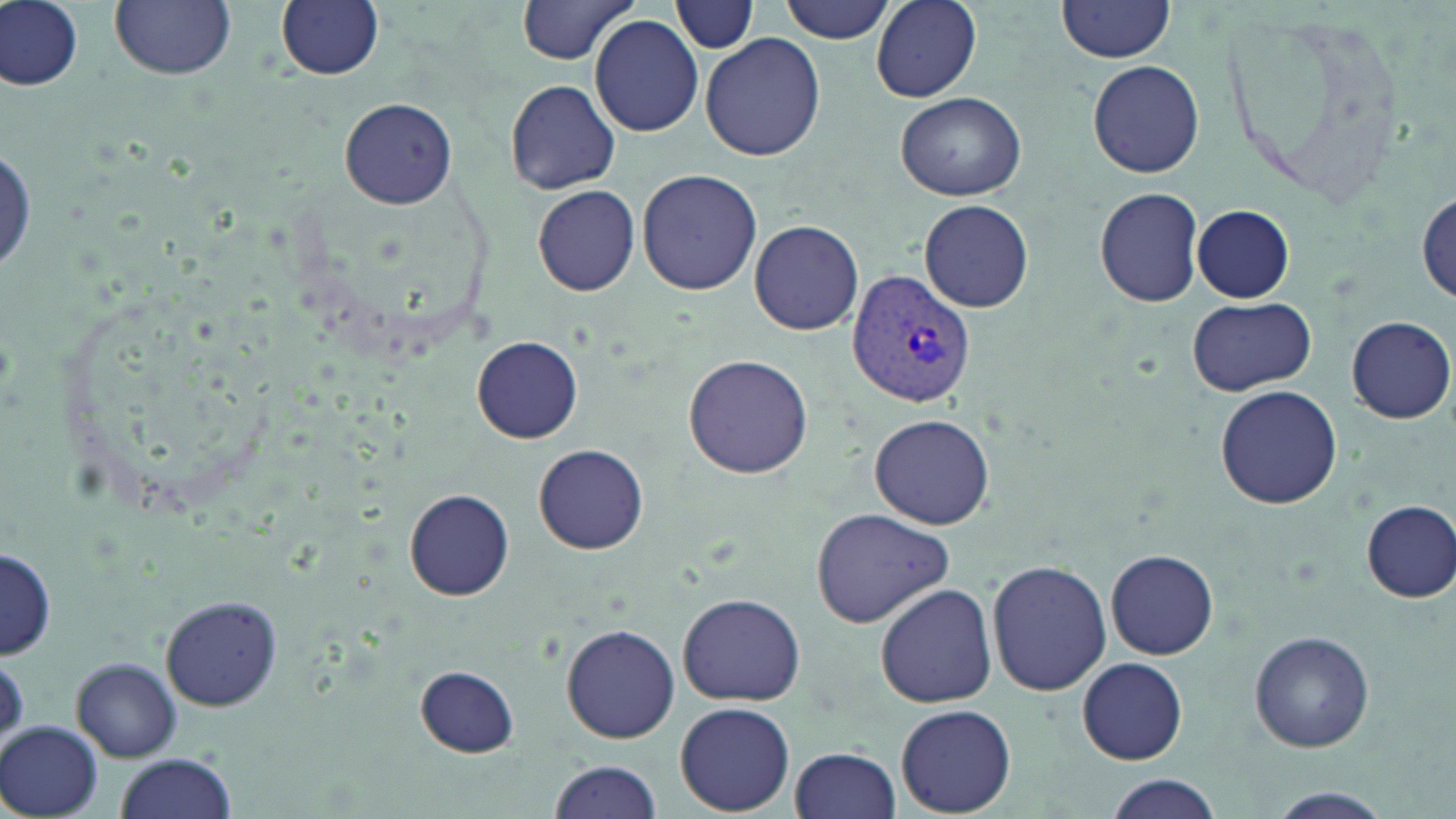

slide-level diagnosis = Plasmodium vivax
modality = light microscopy
preparation = thin blood film
magnification = 1000x
stain = May-Grünwald-Giemsa
uninfected red blood cell locations = approximate bounding boxes as [x1, y1, x2, y2] in pixels: [111, 0, 236, 80], [276, 0, 384, 81], [516, 0, 643, 66], [778, 0, 898, 44], [872, 0, 982, 102], [2, 1, 84, 91], [671, 1, 758, 54], [1058, 1, 1176, 66], [589, 14, 703, 136], [700, 31, 826, 161], [1089, 61, 1204, 178], [504, 78, 621, 195], [894, 90, 1026, 200], [339, 98, 458, 208], [637, 169, 763, 295], [533, 185, 642, 296], [1094, 186, 1205, 308], [1415, 187, 1455, 303], [919, 199, 1035, 313], [1191, 204, 1295, 303], [749, 219, 864, 336], [1187, 298, 1316, 396], [1347, 316, 1455, 423], [473, 335, 583, 443], [683, 353, 814, 479], [1215, 384, 1342, 508], [871, 413, 993, 530], [534, 442, 649, 554], [405, 488, 515, 601], [1361, 500, 1456, 602], [812, 507, 953, 627], [1105, 547, 1218, 659], [0, 548, 56, 660], [986, 559, 1112, 697], [875, 582, 997, 708], [677, 592, 805, 707], [159, 595, 285, 710], [561, 624, 680, 744], [1249, 631, 1376, 752], [1077, 656, 1188, 765], [72, 658, 182, 762], [415, 665, 519, 756], [675, 702, 796, 815], [895, 704, 1016, 817], [1, 721, 104, 818], [788, 746, 901, 819], [114, 752, 238, 819], [546, 758, 663, 818], [1103, 776, 1224, 818], [1257, 786, 1399, 819]
field of view = single
Plasmodium vivax-infected red blood cell locations = approximate bounding boxes as [x1, y1, x2, y2] in pixels: [849, 270, 975, 407]
image size = 1456×819 pixels